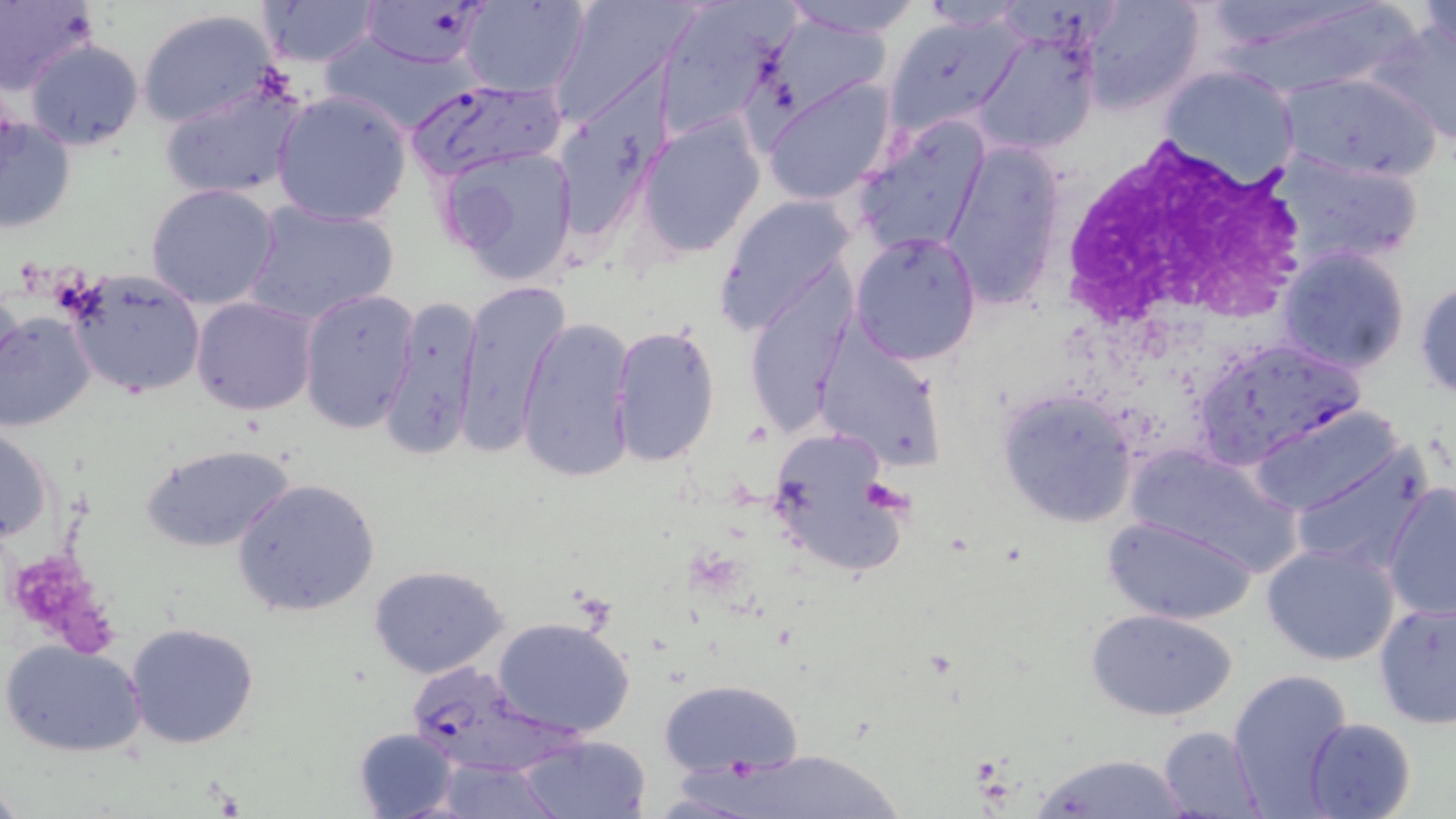

Approximate bounding boxes as [x1, y1, x2, y2] in pixels. Plasmodium falciparum-infected red blood cell locations: [358, 0, 491, 72], [406, 76, 567, 184], [402, 649, 586, 783]. White blood cell locations: [1053, 139, 1308, 351]. Uninfected red blood cell locations: [0, 0, 97, 97], [254, 0, 383, 68], [462, 0, 588, 97], [548, 0, 700, 120], [780, 0, 923, 40], [1081, 0, 1205, 112], [1214, 0, 1413, 101], [1419, 0, 1455, 67], [651, 2, 785, 140], [915, 2, 1033, 31], [136, 8, 283, 130], [766, 13, 889, 112], [881, 15, 1027, 137], [1367, 16, 1456, 146], [972, 26, 1100, 156], [23, 39, 144, 150], [1159, 65, 1301, 188], [1277, 70, 1442, 183], [762, 78, 897, 205], [161, 82, 304, 201], [272, 90, 412, 226], [0, 112, 76, 236], [854, 116, 992, 256], [638, 117, 764, 258], [940, 142, 1065, 309], [437, 143, 580, 286], [1268, 150, 1428, 272], [144, 183, 282, 310], [715, 193, 858, 338], [240, 198, 400, 328], [849, 231, 983, 364], [1276, 246, 1410, 375], [744, 269, 856, 436], [67, 272, 207, 397], [1414, 278, 1456, 401], [459, 281, 569, 449], [298, 288, 419, 435], [376, 294, 482, 463], [191, 297, 317, 416], [0, 310, 97, 431], [516, 316, 636, 482], [609, 323, 722, 468], [812, 333, 949, 471], [1195, 339, 1363, 460], [996, 390, 1141, 528], [1246, 404, 1406, 516], [764, 424, 908, 580], [0, 425, 54, 544], [141, 442, 296, 552], [1289, 443, 1434, 575], [1125, 445, 1303, 576], [234, 478, 381, 618], [1382, 483, 1456, 621], [1103, 516, 1257, 626], [1262, 543, 1401, 666], [369, 565, 511, 680], [1373, 599, 1456, 731], [1084, 607, 1239, 721], [493, 616, 637, 738], [126, 623, 260, 749], [2, 638, 146, 758], [1228, 669, 1357, 816], [657, 677, 804, 779], [1304, 717, 1416, 819], [1157, 725, 1268, 817], [351, 727, 461, 819], [516, 733, 652, 819], [1031, 752, 1199, 818], [432, 760, 563, 817]. Platelet locations: [858, 478, 912, 520], [12, 551, 115, 654]. Slide-level diagnosis: Plasmodium falciparum. Image is 1456×819 pixels. Light microscopy. Captured at 1000x magnification. Thin blood film. May-Grünwald-Giemsa stain. One field of a larger specimen.